Assess this cell for malaria.
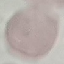

Uninfected.

preparation: thin blood film
stain: Giemsa
image_type: automatically extracted cell patch, resized to 64 × 64 pixels
capture: smartphone camera at the microscope eyepiece